State which parasite is depicted.
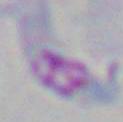

Toxoplasma gondii.

magnification = 1000x
modality = micrograph